Comment on the morphology of the erythrocytes.
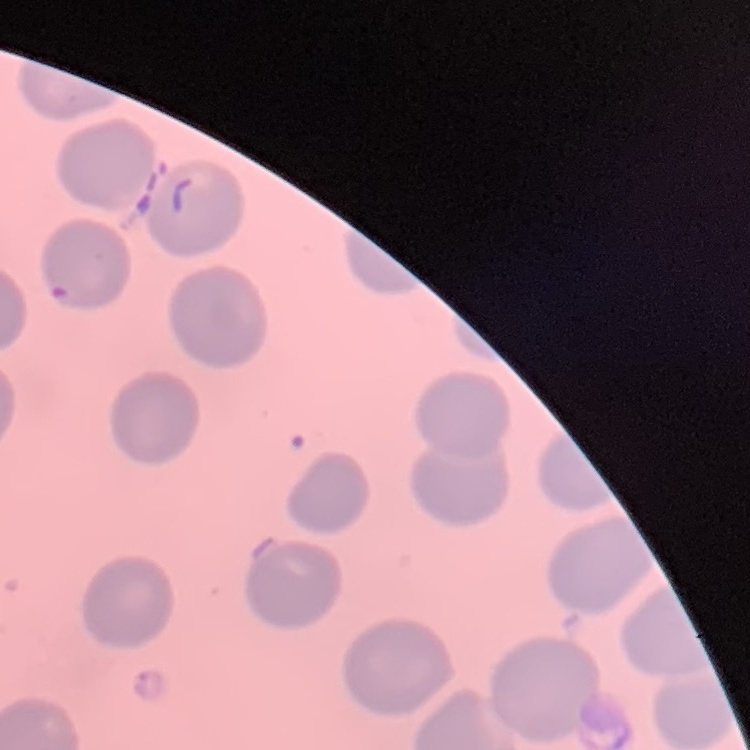
They show no rouleaux formation.

image_type: square crop of a larger photomicrograph
stain: Field's or Giemsa
preparation: thin blood smear